Locate and identify every blood parasite.
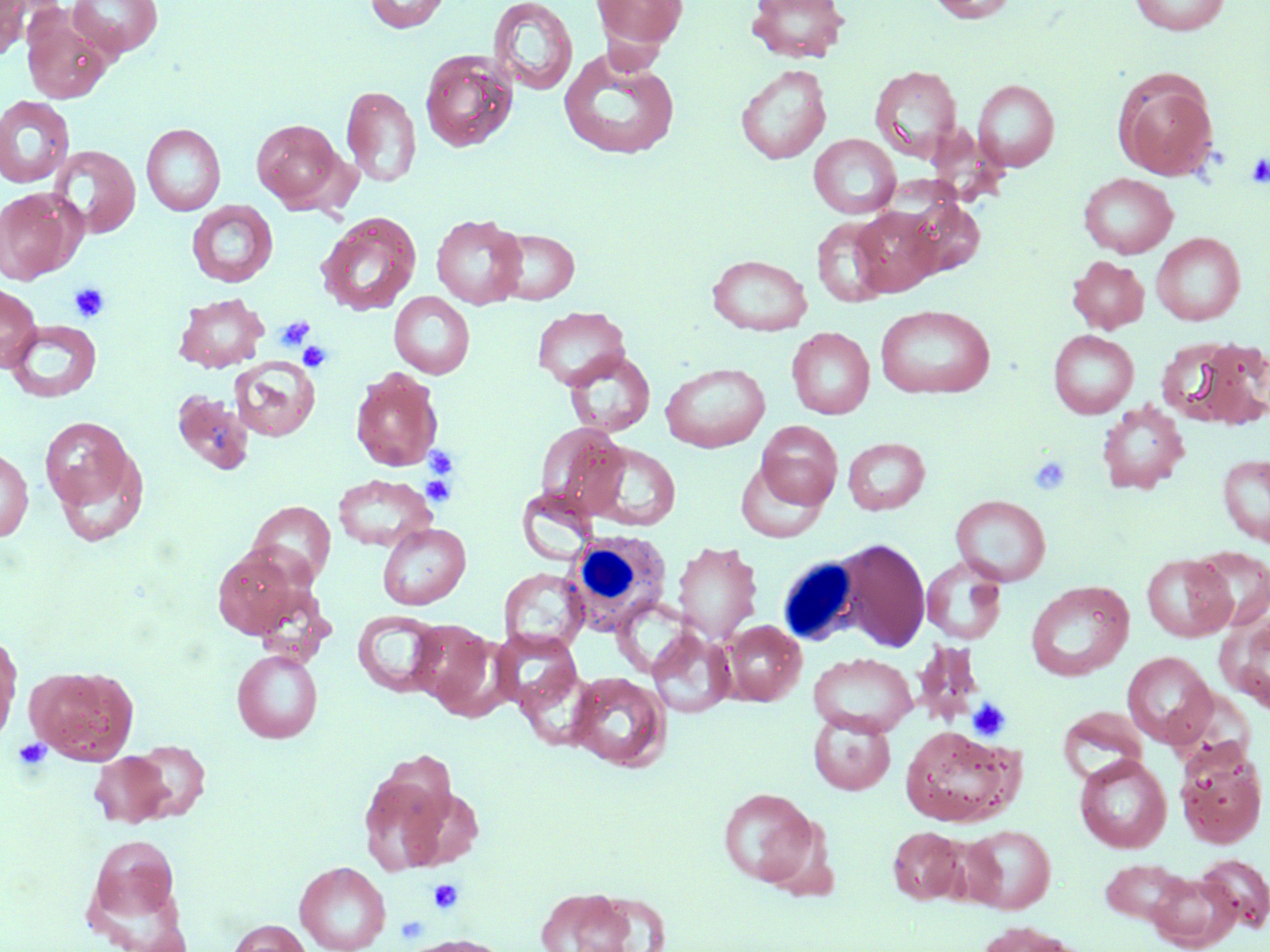

No blood parasites observed.

{
  "slide_level_diagnosis": "negative for blood parasites",
  "uninfected_red_blood_cell_locations": "approximate bounding boxes as (x1, y1, x2, y2) in pixels: (0, 0, 29, 61), (363, 0, 450, 33), (487, 0, 578, 96), (591, 0, 688, 52), (746, 0, 851, 63), (924, 0, 1020, 23), (1128, 0, 1232, 36), (68, 1, 163, 59), (22, 9, 113, 103), (559, 48, 680, 160), (420, 50, 517, 152), (735, 64, 831, 164), (869, 65, 962, 163), (1112, 68, 1219, 181), (973, 79, 1059, 171), (341, 85, 421, 188), (0, 96, 75, 188), (250, 118, 350, 210), (141, 123, 226, 216), (809, 134, 900, 219), (48, 145, 140, 239), (1078, 172, 1178, 258), (0, 188, 85, 284), (898, 196, 985, 281), (186, 201, 278, 287), (851, 207, 942, 296), (316, 213, 422, 316), (431, 214, 526, 309), (812, 216, 894, 307), (491, 228, 579, 304), (1151, 232, 1245, 325), (707, 254, 812, 335), (1067, 255, 1150, 334), (0, 283, 41, 372), (389, 292, 475, 379), (173, 293, 270, 373), (876, 304, 995, 399), (532, 306, 629, 390), (5, 320, 102, 402), (787, 327, 874, 419), (1048, 329, 1138, 418), (1166, 336, 1270, 428), (563, 350, 655, 436), (229, 357, 320, 442), (660, 363, 770, 452), (350, 367, 444, 472), (171, 392, 255, 475), (1096, 401, 1190, 494), (40, 416, 138, 516), (757, 420, 844, 508), (536, 422, 629, 518), (843, 437, 930, 515), (587, 442, 680, 530), (0, 447, 33, 542), (50, 447, 150, 548), (1217, 453, 1270, 546), (735, 461, 829, 543), (333, 474, 436, 551), (517, 488, 600, 565), (951, 495, 1051, 585), (247, 501, 336, 588), (377, 523, 471, 610), (834, 538, 930, 651), (672, 541, 763, 643), (1189, 546, 1270, 631), (211, 547, 309, 639), (1141, 554, 1235, 642), (921, 556, 1008, 645), (499, 567, 588, 651), (1025, 581, 1134, 682), (353, 611, 445, 697), (1218, 613, 1270, 713), (410, 620, 498, 713), (722, 620, 806, 706), (647, 628, 735, 718), (491, 630, 581, 712), (0, 639, 19, 744), (913, 642, 986, 726), (232, 650, 322, 743), (1122, 651, 1217, 749), (808, 652, 917, 735), (517, 665, 597, 750), (25, 666, 139, 764), (567, 672, 670, 771), (1058, 706, 1150, 782), (808, 712, 895, 795), (899, 724, 1023, 827), (131, 740, 210, 821), (1174, 742, 1268, 849), (90, 752, 173, 827), (1074, 754, 1172, 853), (357, 762, 459, 875), (717, 788, 819, 887), (962, 825, 1057, 913), (888, 826, 965, 904), (86, 834, 182, 930), (1197, 853, 1270, 932), (1098, 858, 1198, 929), (295, 861, 391, 952), (1143, 869, 1241, 951), (534, 886, 649, 952), (227, 919, 311, 952), (973, 921, 1083, 952), (401, 935, 512, 952)",
  "image_size": "1270×952 pixels",
  "field_of_view": "single",
  "stain": "May-Grünwald-Giemsa",
  "preparation": "thin blood film",
  "modality": "optical microscopy",
  "magnification": "1000x",
  "platelet_locations": "approximate bounding boxes as (x1, y1, x2, y2) in pixels: (1246, 154, 1270, 188), (69, 281, 110, 322), (275, 315, 315, 351), (298, 341, 333, 372), (425, 446, 460, 480), (1028, 455, 1072, 495), (422, 474, 458, 507), (968, 698, 1011, 741), (13, 737, 51, 771), (428, 878, 464, 915), (396, 915, 429, 945)",
  "white_blood_cell_locations": "approximate bounding boxes as (x1, y1, x2, y2) in pixels: (566, 530, 671, 633), (776, 556, 864, 647)"
}